Classify this cell by malaria status.
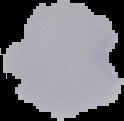
Parasitized.

image size = 124×121 pixels
preparation = thin blood film
image type = cell region segmented out of the field of view; surrounding area masked to black